Give the position of every Plasmodium parasite, noting whether each is a trophozoite, schizont, or gametocyte.
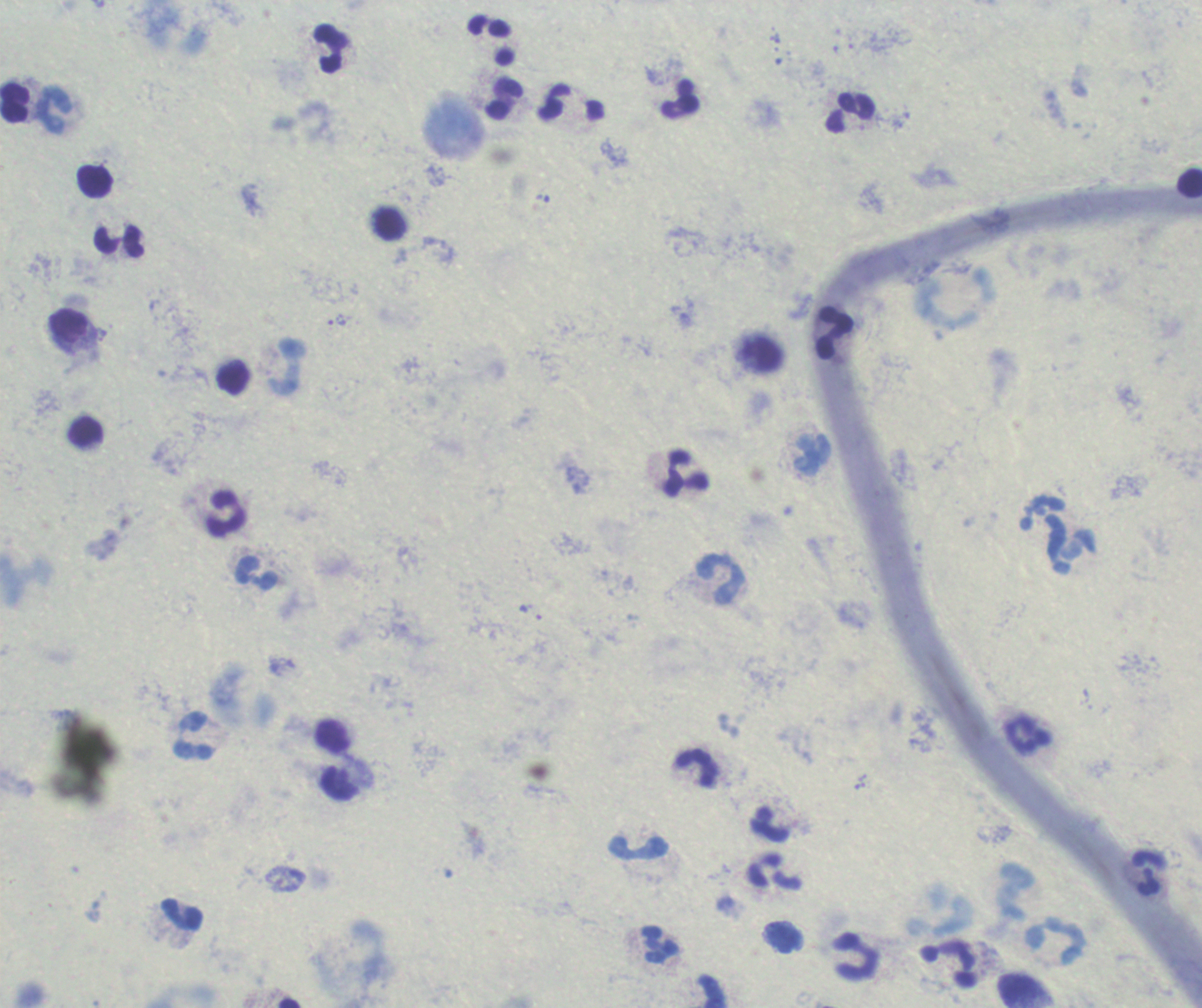

Approximate centers as [x, y] in pixels.
Trophozoites: [337, 320].
No schizont or gametocyte forms observed.

coordinate format = approximate centers as [x, y] in pixels
leukocyte locations = [492, 41], [331, 48], [681, 98], [505, 99], [15, 103], [571, 103], [54, 110], [851, 112], [95, 182], [1190, 183], [120, 243], [69, 325], [834, 332], [761, 354], [286, 367], [85, 432], [813, 453], [686, 474], [226, 513], [1071, 545], [256, 573], [720, 580], [1029, 733], [194, 736], [333, 736], [697, 768], [769, 825], [638, 847], [775, 873], [1149, 874], [183, 914], [1057, 940], [660, 944], [856, 957], [948, 964], [1027, 991], [711, 992]
field of view = single
image size = 1202×1008 pixels
background quality = poor
context = previously used in an actual diagnosis
preparation = thick smear of blood
magnification = 100x
stain = Romanowsky